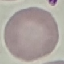

Summary:
  - Result: no malaria parasites seen
  - Capture: smartphone camera at the microscope eyepiece
  - Stain: Giemsa
  - Image type: cell patch, automatically extracted from a larger field of view and resized to 64 × 64 pixels
  - Preparation: thin blood film